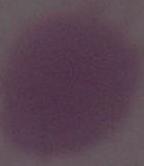
Summary:
  - Identification: erythrocyte
  - Modality: micrograph
  - Magnification: 1000x